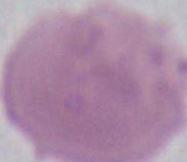 Photomicrograph. An erythrocyte is shown. Captured at 1000x magnification.